Classify this cell by malaria status.
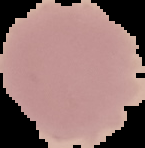

It is uninfected.

Cell region segmented out of the field of view; the surrounding area is masked to black. Image is 145×148 pixels. From a thin blood film.